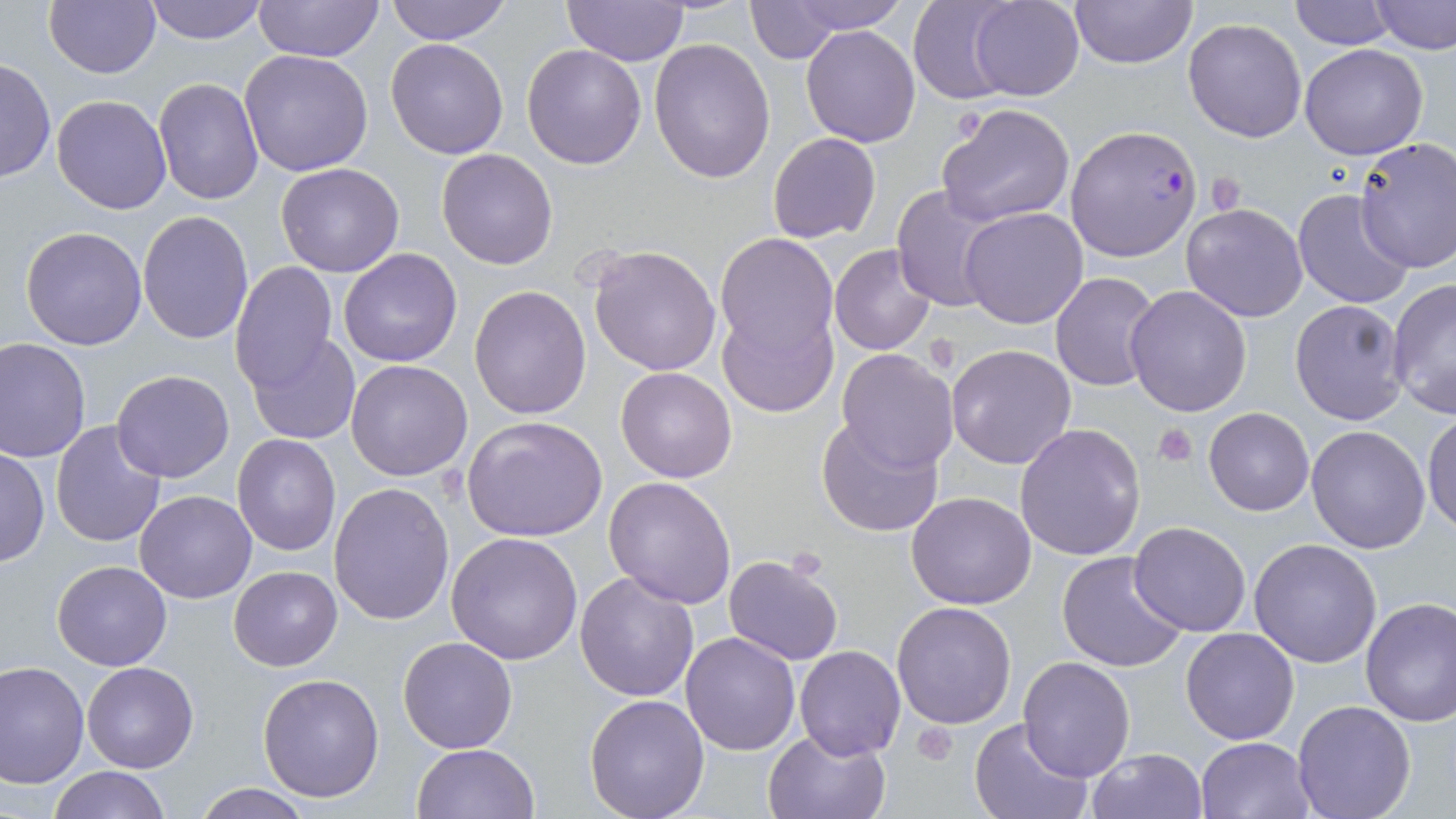
Summary:
  - Coordinate format: approximate bounding boxes as named x1/y1/x2/y2 corners in pixels
  - Plasmodium falciparum-infected red blood cell locations: (x1=1065, y1=124, x2=1203, y2=262)
  - Platelet locations: (x1=952, y1=104, x2=988, y2=145), (x1=1206, y1=172, x2=1246, y2=216), (x1=1152, y1=422, x2=1198, y2=467), (x1=912, y1=720, x2=958, y2=764)
  - Uninfected red blood cell locations: (x1=44, y1=0, x2=161, y2=79), (x1=141, y1=0, x2=270, y2=44), (x1=253, y1=0, x2=384, y2=65), (x1=384, y1=0, x2=512, y2=45), (x1=777, y1=0, x2=912, y2=34), (x1=904, y1=0, x2=1024, y2=104), (x1=969, y1=0, x2=1085, y2=100), (x1=1068, y1=0, x2=1200, y2=70), (x1=1289, y1=0, x2=1394, y2=48), (x1=1370, y1=0, x2=1456, y2=54), (x1=562, y1=1, x2=689, y2=67), (x1=741, y1=3, x2=846, y2=62), (x1=1183, y1=17, x2=1308, y2=141), (x1=801, y1=25, x2=920, y2=148), (x1=385, y1=37, x2=509, y2=158), (x1=649, y1=37, x2=778, y2=183), (x1=522, y1=43, x2=648, y2=168), (x1=1299, y1=43, x2=1428, y2=160), (x1=239, y1=49, x2=373, y2=176), (x1=1, y1=57, x2=55, y2=185), (x1=153, y1=78, x2=265, y2=205), (x1=51, y1=94, x2=172, y2=215), (x1=938, y1=102, x2=1078, y2=227), (x1=768, y1=132, x2=881, y2=244), (x1=1354, y1=138, x2=1456, y2=273), (x1=436, y1=148, x2=557, y2=270), (x1=274, y1=162, x2=404, y2=276), (x1=891, y1=183, x2=1009, y2=315), (x1=1291, y1=188, x2=1416, y2=311), (x1=1181, y1=203, x2=1310, y2=321), (x1=960, y1=206, x2=1089, y2=329), (x1=136, y1=212, x2=254, y2=343), (x1=20, y1=226, x2=148, y2=349), (x1=715, y1=232, x2=835, y2=355), (x1=587, y1=243, x2=724, y2=376), (x1=829, y1=243, x2=938, y2=357), (x1=338, y1=248, x2=464, y2=367), (x1=230, y1=261, x2=340, y2=393), (x1=1049, y1=273, x2=1160, y2=391), (x1=1386, y1=275, x2=1456, y2=418), (x1=1124, y1=285, x2=1252, y2=416), (x1=469, y1=286, x2=592, y2=420), (x1=1290, y1=298, x2=1409, y2=426), (x1=715, y1=301, x2=837, y2=418), (x1=246, y1=332, x2=361, y2=444), (x1=0, y1=338, x2=92, y2=462), (x1=946, y1=343, x2=1077, y2=469), (x1=836, y1=348, x2=958, y2=471), (x1=346, y1=359, x2=473, y2=481), (x1=616, y1=366, x2=737, y2=482), (x1=111, y1=369, x2=235, y2=482), (x1=1204, y1=406, x2=1314, y2=515), (x1=1422, y1=409, x2=1456, y2=538), (x1=462, y1=416, x2=608, y2=542), (x1=816, y1=416, x2=944, y2=538), (x1=49, y1=420, x2=167, y2=549), (x1=1014, y1=423, x2=1145, y2=561), (x1=1306, y1=424, x2=1432, y2=553), (x1=232, y1=434, x2=340, y2=555), (x1=1, y1=448, x2=49, y2=567), (x1=604, y1=476, x2=736, y2=608), (x1=328, y1=481, x2=455, y2=624), (x1=135, y1=490, x2=256, y2=603), (x1=906, y1=491, x2=1037, y2=609), (x1=1129, y1=521, x2=1252, y2=637), (x1=447, y1=531, x2=584, y2=666), (x1=1249, y1=538, x2=1384, y2=667), (x1=1056, y1=551, x2=1188, y2=675), (x1=723, y1=553, x2=844, y2=666), (x1=52, y1=561, x2=173, y2=670), (x1=229, y1=565, x2=342, y2=670), (x1=575, y1=571, x2=701, y2=701), (x1=1359, y1=597, x2=1456, y2=727), (x1=891, y1=601, x2=1017, y2=729), (x1=1181, y1=627, x2=1299, y2=745), (x1=680, y1=631, x2=800, y2=755), (x1=397, y1=636, x2=519, y2=754), (x1=793, y1=645, x2=906, y2=761), (x1=1019, y1=656, x2=1136, y2=782), (x1=82, y1=661, x2=199, y2=772), (x1=0, y1=662, x2=91, y2=789), (x1=257, y1=673, x2=385, y2=802), (x1=584, y1=694, x2=710, y2=817), (x1=1292, y1=700, x2=1417, y2=819), (x1=968, y1=716, x2=1092, y2=819), (x1=763, y1=728, x2=890, y2=818), (x1=1196, y1=736, x2=1315, y2=819), (x1=411, y1=743, x2=539, y2=819), (x1=1086, y1=747, x2=1207, y2=819), (x1=47, y1=766, x2=170, y2=819), (x1=191, y1=782, x2=317, y2=818)
  - Slide-level diagnosis: Plasmodium falciparum
  - Preparation: thin blood film
  - Magnification: 1000x
  - Image size: 1456×819 pixels
  - Stain: May-Grünwald-Giemsa
  - Field of view: single
  - Modality: light microscopy